Identify the parasite.
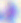

This is Toxoplasma gondii.

Captured at 400x magnification. Micrograph.